Classify this cell by malaria status.
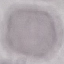

Uninfected.

Thin smear of blood. Giemsa-stained preparation. Cell patch, automatically extracted from a larger field of view and resized to 64 × 64 pixels. Photographed with a smartphone camera at the microscope eyepiece.